Identify the cell.
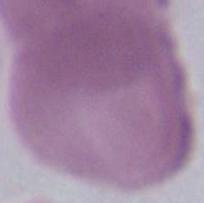

An erythrocyte.

Captured at 1000x magnification. Micrograph.